Assess this cell for malaria.
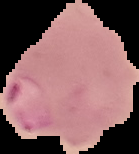
It is parasitized.

Image is 139×154 pixels. From a thin blood smear. Cell region segmented out of the field of view; the surrounding area is masked to black.